Locate every Plasmodium falciparum parasite and give its life-cycle stage, and locate every leukocyte and any debris.
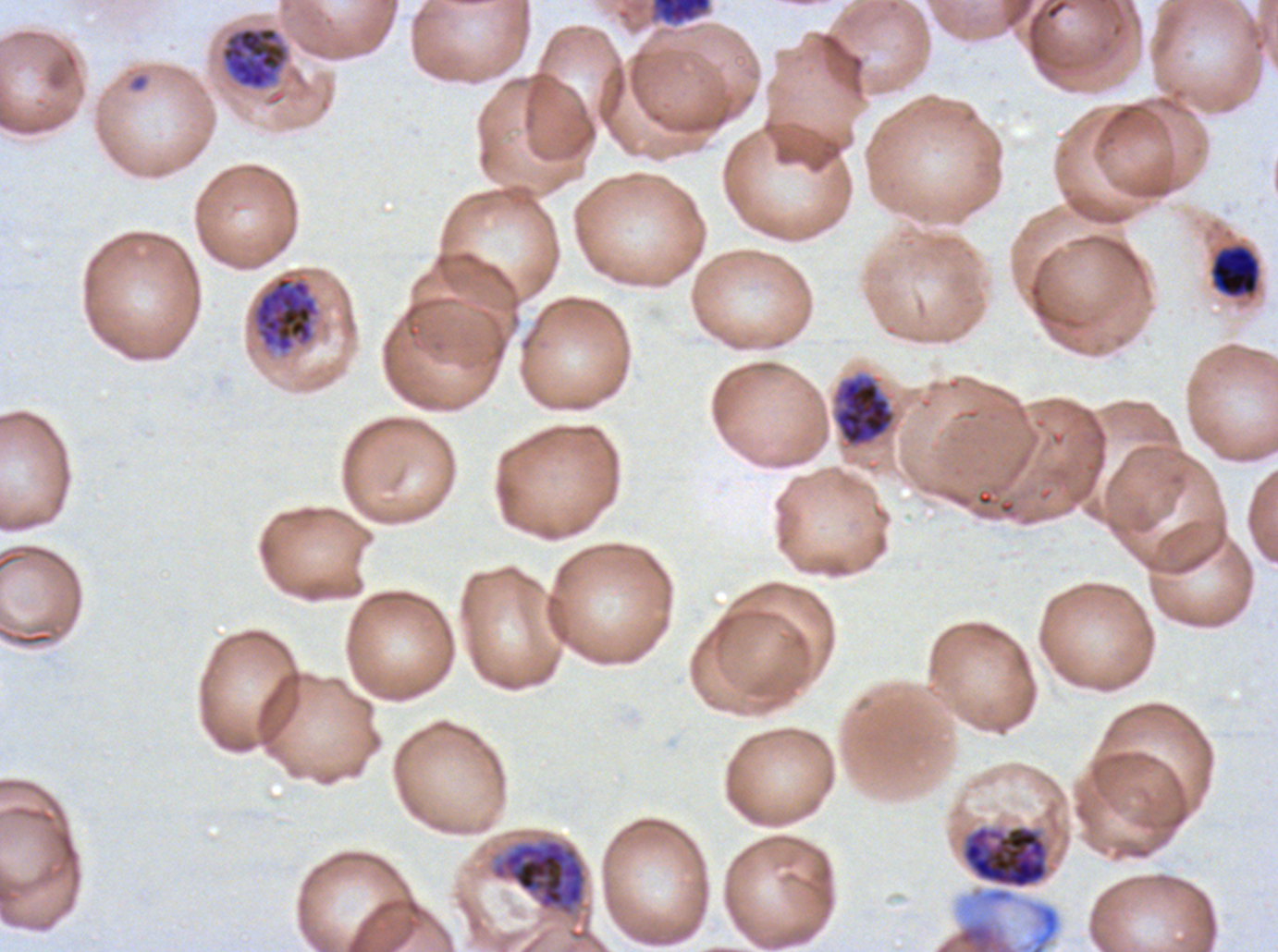

Approximate bounding boxes as [x1, y1, x2, y2] in pixels.
Rings: [128, 72, 150, 93].
Mid trophozoites: [1210, 244, 1260, 298].
Early schizonts: [220, 26, 289, 91], [246, 267, 325, 361], [961, 824, 1050, 890], [463, 825, 612, 951].
Late schizonts: [651, 0, 712, 25], [833, 374, 895, 446].
No late-ring/early-trophozoite forms, late trophozoites, segmenters, gametocytes, leukocytes, or debris observed.

stain = Giemsa
life-cycle stages observed = ring, mid trophozoite, early schizont, late schizont
specimen = Plasmodium falciparum cultured ex vivo for 24 to 48 hours, from a patient in The Gambia
image size = 1278×952 pixels
preparation = thin blood film
field of view = one sub-image of a larger composite